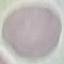
result: no malaria parasites seen
stain: Giemsa
image_type: cell patch, automatically extracted from a larger field of view and resized to 64 × 64 pixels
capture: smartphone camera at the microscope eyepiece
preparation: thin smear